Report the malaria status.
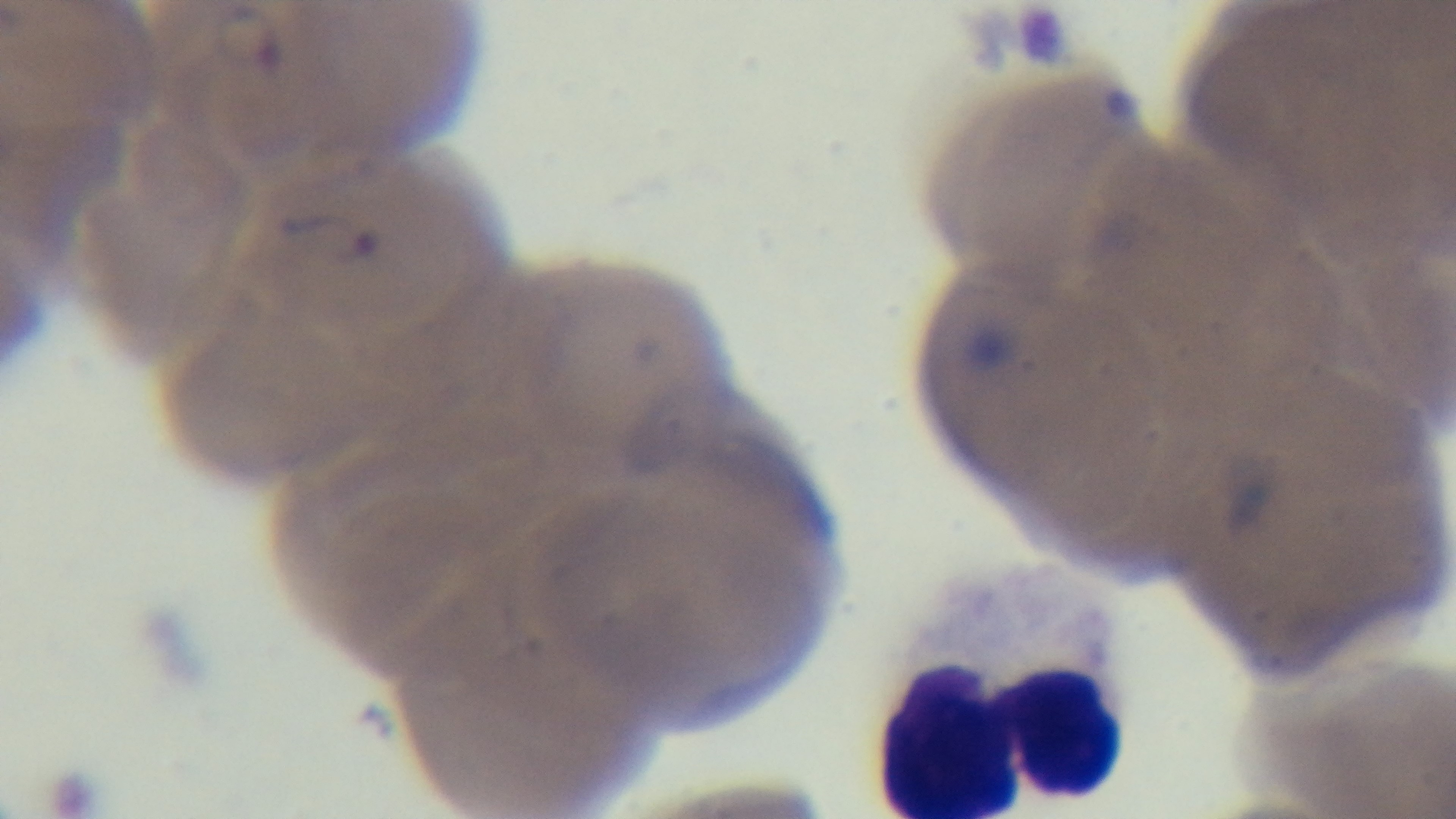

Infected.

objective = 100x oil immersion
stain = Giemsa
capture = mounted 4K digital camera
field of view = one from the slide
modality = light microscopy
preparation = thin